Outline each uninfected red blood cell.
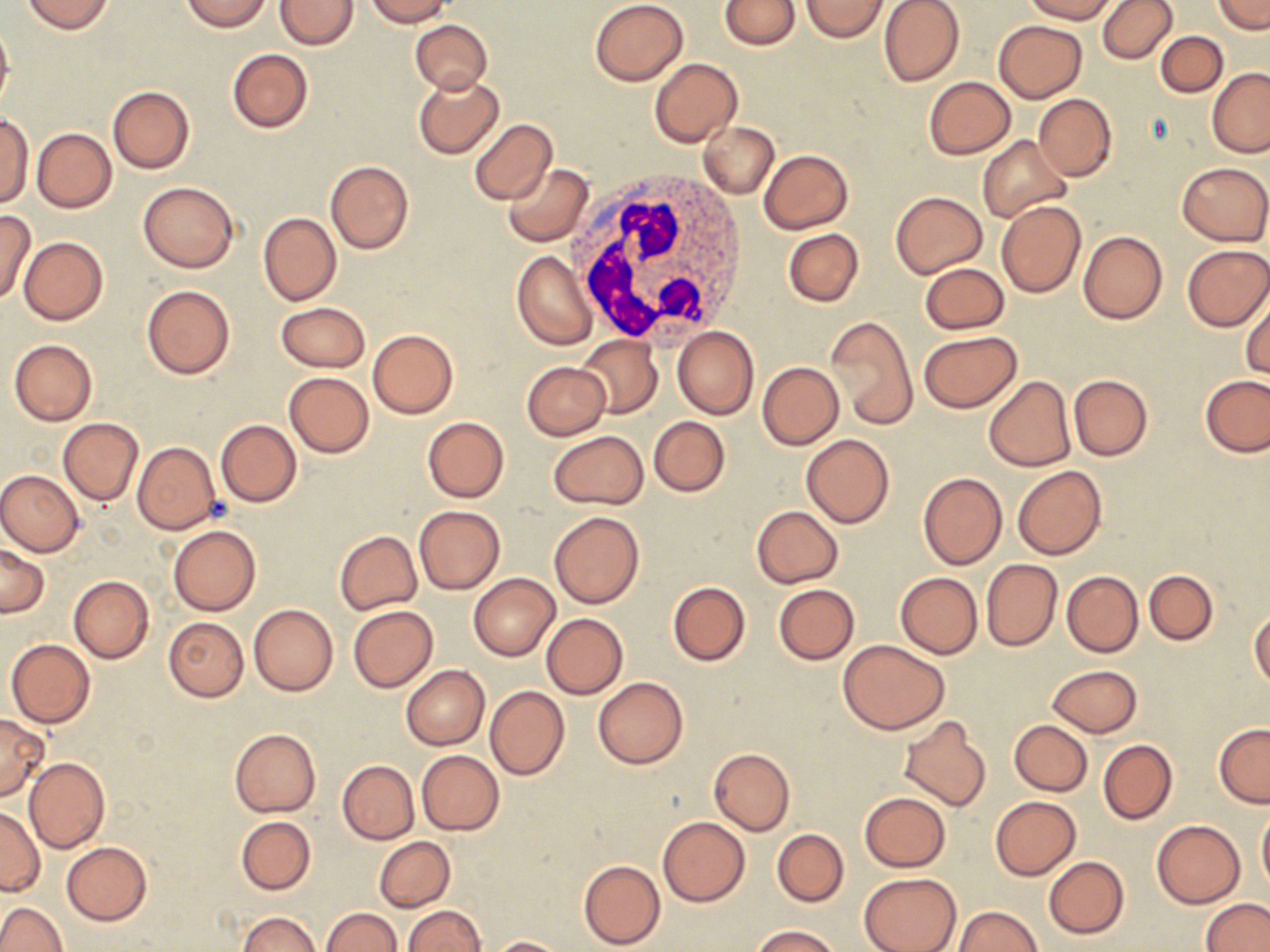

Approximate bounding boxes as named x1/y1/x2/y2 corners in pixels.
Uninfected red blood cells: (x1=21, y1=0, x2=114, y2=34), (x1=180, y1=0, x2=271, y2=30), (x1=276, y1=0, x2=359, y2=49), (x1=365, y1=0, x2=453, y2=26), (x1=590, y1=0, x2=688, y2=86), (x1=719, y1=0, x2=799, y2=51), (x1=801, y1=0, x2=889, y2=41), (x1=879, y1=0, x2=966, y2=87), (x1=1023, y1=0, x2=1119, y2=22), (x1=1097, y1=0, x2=1177, y2=65), (x1=1213, y1=0, x2=1268, y2=34), (x1=0, y1=17, x2=14, y2=112), (x1=408, y1=19, x2=492, y2=94), (x1=994, y1=19, x2=1086, y2=102), (x1=1156, y1=31, x2=1228, y2=96), (x1=227, y1=49, x2=313, y2=133), (x1=648, y1=57, x2=743, y2=148), (x1=1207, y1=69, x2=1270, y2=158), (x1=412, y1=73, x2=504, y2=159), (x1=924, y1=76, x2=1016, y2=160), (x1=107, y1=85, x2=195, y2=174), (x1=1034, y1=94, x2=1117, y2=182), (x1=0, y1=114, x2=33, y2=207), (x1=469, y1=119, x2=556, y2=206), (x1=699, y1=121, x2=779, y2=199), (x1=31, y1=128, x2=116, y2=212), (x1=978, y1=135, x2=1072, y2=223), (x1=760, y1=149, x2=853, y2=233), (x1=325, y1=160, x2=414, y2=255), (x1=1179, y1=162, x2=1269, y2=245), (x1=502, y1=163, x2=594, y2=247), (x1=138, y1=180, x2=239, y2=272), (x1=891, y1=191, x2=988, y2=278), (x1=996, y1=201, x2=1086, y2=298), (x1=0, y1=210, x2=36, y2=304), (x1=258, y1=212, x2=340, y2=306), (x1=784, y1=229, x2=863, y2=307), (x1=1078, y1=231, x2=1167, y2=324), (x1=19, y1=237, x2=108, y2=326), (x1=1182, y1=244, x2=1270, y2=331), (x1=512, y1=251, x2=597, y2=350), (x1=919, y1=262, x2=1009, y2=335), (x1=141, y1=284, x2=235, y2=378), (x1=1241, y1=294, x2=1270, y2=380), (x1=275, y1=302, x2=369, y2=373), (x1=824, y1=314, x2=917, y2=430), (x1=673, y1=326, x2=759, y2=419), (x1=368, y1=329, x2=458, y2=419), (x1=918, y1=332, x2=1024, y2=413), (x1=577, y1=333, x2=663, y2=419), (x1=9, y1=339, x2=97, y2=425), (x1=521, y1=362, x2=611, y2=440), (x1=757, y1=362, x2=843, y2=450), (x1=285, y1=372, x2=373, y2=457), (x1=1069, y1=373, x2=1153, y2=462), (x1=983, y1=376, x2=1074, y2=471), (x1=1201, y1=376, x2=1269, y2=456), (x1=421, y1=416, x2=509, y2=502), (x1=58, y1=417, x2=143, y2=504), (x1=649, y1=417, x2=730, y2=497), (x1=216, y1=420, x2=301, y2=507), (x1=547, y1=431, x2=649, y2=511), (x1=801, y1=434, x2=894, y2=528), (x1=132, y1=442, x2=222, y2=535), (x1=1012, y1=465, x2=1106, y2=560), (x1=0, y1=470, x2=85, y2=556), (x1=917, y1=472, x2=1007, y2=569), (x1=414, y1=505, x2=505, y2=595), (x1=751, y1=505, x2=843, y2=588), (x1=549, y1=511, x2=645, y2=609), (x1=168, y1=525, x2=260, y2=615), (x1=334, y1=530, x2=422, y2=614), (x1=0, y1=545, x2=49, y2=618), (x1=980, y1=559, x2=1062, y2=652), (x1=1144, y1=569, x2=1218, y2=645), (x1=1061, y1=571, x2=1144, y2=657), (x1=895, y1=572, x2=983, y2=659), (x1=468, y1=573, x2=559, y2=661), (x1=69, y1=575, x2=155, y2=662), (x1=668, y1=581, x2=751, y2=666), (x1=772, y1=584, x2=859, y2=664), (x1=248, y1=604, x2=337, y2=696), (x1=348, y1=605, x2=439, y2=692), (x1=1250, y1=608, x2=1270, y2=691), (x1=541, y1=613, x2=627, y2=698), (x1=164, y1=617, x2=250, y2=701), (x1=6, y1=639, x2=95, y2=727), (x1=839, y1=641, x2=949, y2=734), (x1=1047, y1=664, x2=1142, y2=736), (x1=402, y1=666, x2=489, y2=749), (x1=592, y1=677, x2=688, y2=769), (x1=485, y1=685, x2=569, y2=780), (x1=0, y1=713, x2=48, y2=802), (x1=898, y1=716, x2=992, y2=814), (x1=1010, y1=720, x2=1092, y2=795), (x1=1214, y1=723, x2=1270, y2=807), (x1=229, y1=728, x2=320, y2=817), (x1=1098, y1=739, x2=1177, y2=824), (x1=708, y1=747, x2=795, y2=834), (x1=417, y1=751, x2=504, y2=835), (x1=24, y1=756, x2=110, y2=854), (x1=337, y1=760, x2=419, y2=845), (x1=859, y1=791, x2=951, y2=872), (x1=990, y1=796, x2=1081, y2=879), (x1=0, y1=805, x2=44, y2=896), (x1=1257, y1=805, x2=1270, y2=895), (x1=657, y1=815, x2=749, y2=907), (x1=236, y1=816, x2=315, y2=894), (x1=1151, y1=819, x2=1245, y2=908), (x1=772, y1=828, x2=849, y2=906), (x1=374, y1=837, x2=455, y2=912), (x1=60, y1=842, x2=151, y2=925), (x1=1043, y1=856, x2=1129, y2=939), (x1=579, y1=860, x2=665, y2=949), (x1=858, y1=872, x2=961, y2=952), (x1=1202, y1=898, x2=1269, y2=952), (x1=0, y1=901, x2=65, y2=951), (x1=403, y1=905, x2=485, y2=952), (x1=952, y1=906, x2=1042, y2=951), (x1=320, y1=907, x2=401, y2=951), (x1=240, y1=913, x2=323, y2=952), (x1=752, y1=925, x2=840, y2=951), (x1=487, y1=936, x2=571, y2=951).

slide_level_diagnosis: no evidence of blood parasites
stain: May-Grünwald-Giemsa
image_size: 1270×952 pixels
magnification: 1000x
field_of_view: one of a larger specimen
white_blood_cell_locations: 'approximate bounding boxes as named x1/y1/x2/y2 corners in pixels: (x1=571, y1=171, x2=753, y2=350)'
preparation: thin blood film
modality: optical microscopy